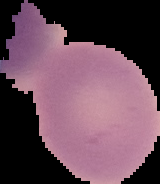
image size = 160×184 pixels
preparation = thin blood smear
result = negative for malaria parasites
image type = cell region segmented out of the field of view; surrounding area masked to black